Give the extent of all uninfected red blood cells.
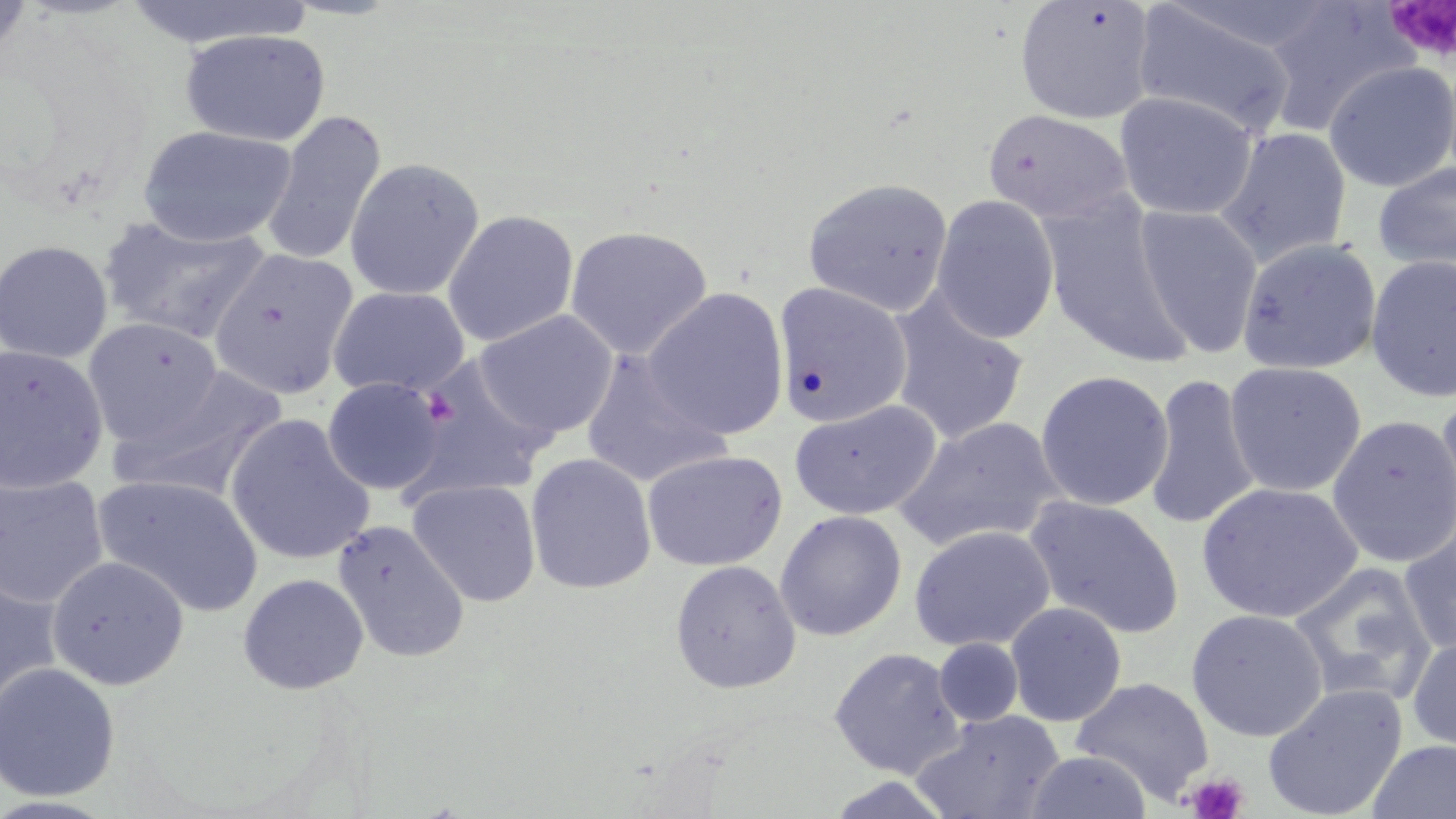
Approximate bounding boxes as (x1,y1)-(x2,y2) corner pairs in pixels.
Uninfected red blood cells: (0,0)-(35,66), (118,0)-(314,50), (1015,0)-(1157,125), (1131,1)-(1300,139), (1261,2)-(1415,136), (179,28)-(331,147), (1323,61)-(1456,192), (1114,91)-(1259,221), (982,108)-(1134,225), (260,111)-(386,268), (137,125)-(297,247), (1214,126)-(1352,267), (343,158)-(485,301), (1372,159)-(1456,273), (803,177)-(954,317), (931,193)-(1060,344), (1038,199)-(1192,367), (1133,204)-(1264,358), (442,209)-(579,346), (97,214)-(271,345), (565,224)-(714,359), (1236,238)-(1383,376), (0,239)-(113,364), (209,249)-(358,400), (1365,254)-(1456,403), (774,282)-(913,428), (328,286)-(469,398), (642,287)-(790,439), (887,291)-(1029,445), (473,310)-(619,439), (83,317)-(223,445), (1,344)-(109,493), (580,350)-(732,489), (405,359)-(554,500), (1223,360)-(1367,497), (108,367)-(286,502), (1035,370)-(1175,511), (1144,373)-(1261,532), (322,377)-(446,495), (1434,392)-(1456,541), (790,398)-(941,521), (224,412)-(376,566), (1326,414)-(1456,568), (893,416)-(1066,551), (642,449)-(787,572), (525,452)-(657,594), (0,473)-(110,608), (92,474)-(264,617), (408,479)-(541,607), (1197,482)-(1363,624), (1023,495)-(1185,639), (774,509)-(907,642), (1399,513)-(1456,658), (332,518)-(470,664), (908,525)-(1055,652), (46,555)-(190,690), (669,559)-(802,694), (1289,561)-(1438,707), (0,568)-(64,723), (238,573)-(369,695), (1005,601)-(1127,726), (1186,608)-(1328,742), (1408,631)-(1456,760), (934,638)-(1023,727), (829,646)-(966,778), (0,661)-(121,802), (1070,676)-(1215,805), (1262,682)-(1409,819), (913,710)-(1065,819), (1366,739)-(1456,819), (1024,749)-(1153,819).

slide-level diagnosis = no evidence of blood parasites
field of view = one of a larger specimen
image size = 1456×819 pixels
magnification = 1000x
modality = optical microscopy
stain = May-Grünwald-Giemsa
preparation = thin blood smear
platelet locations = approximate bounding boxes as (x1,y1)-(x2,y2) corner pairs in pixels: (1383,1)-(1456,65), (420,388)-(459,427), (1184,772)-(1250,819)